Comment on the morphology of the erythrocytes.
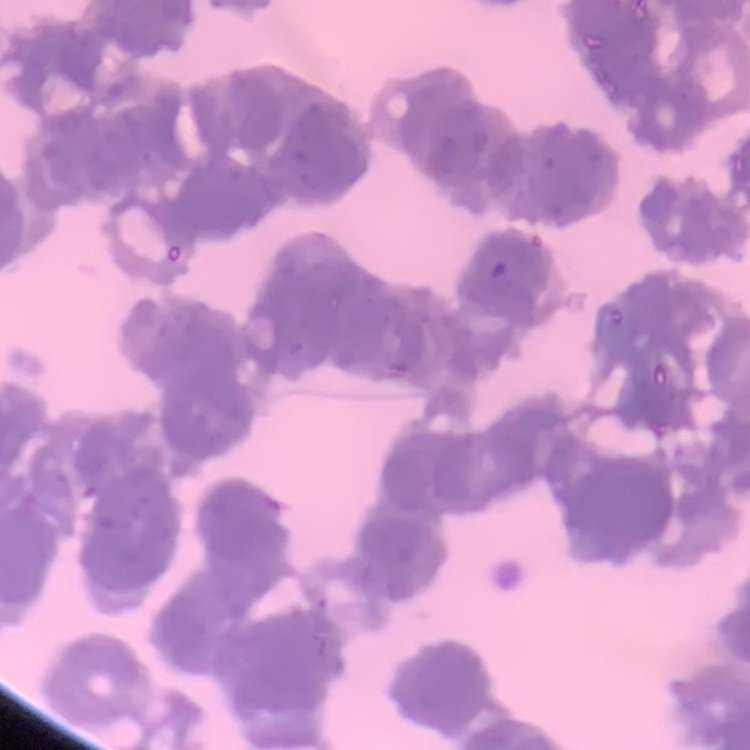

They show rouleaux formation.

{
  "stain": "Field's or Giemsa",
  "image_type": "one tile cut from a larger photomicrograph",
  "preparation": "thin peripheral smear"
}